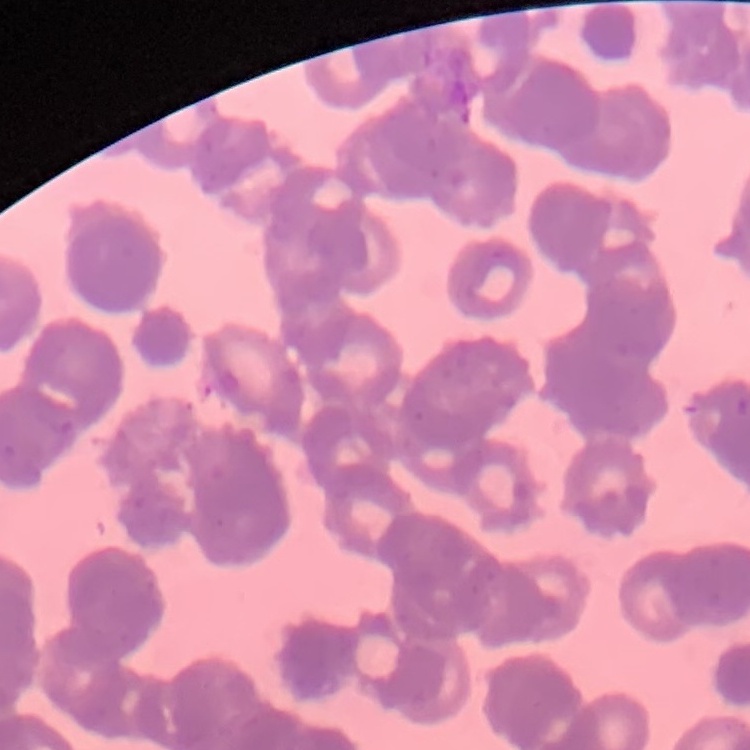
{
  "red_blood_cell_morphology": "rouleaux formation",
  "image_type": "square crop of a larger photomicrograph",
  "stain": "Field's or Giemsa",
  "preparation": "thin blood smear"
}